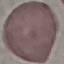
Malaria status: uninfected. Thin blood smear. Automatically extracted cell patch, resized to 64 × 64 pixels. Giemsa-stained preparation. Acquired by smartphone through the microscope eyepiece.